Assess this cell for malaria.
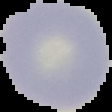
It is uninfected.

preparation = thin blood film
image size = 112×112 pixels
image type = cell region segmented out of the field of view; surrounding area masked to black